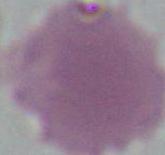
magnification = 1000x
identification = erythrocyte
modality = photomicrograph